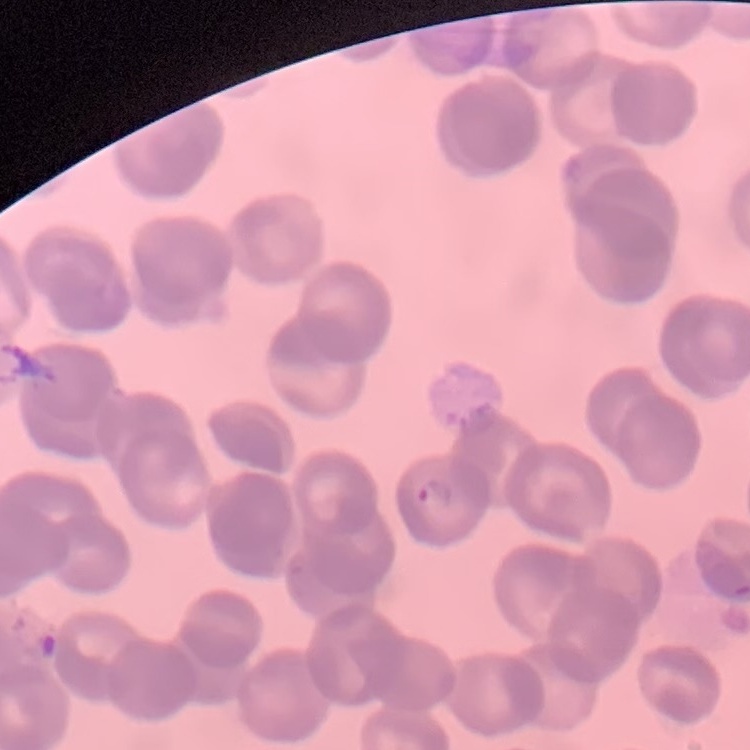 The red blood cells show rouleaux formation. Stained with either Field's or Giemsa. Thin blood smear. One tile cut from a larger photomicrograph.